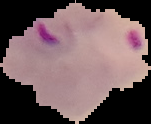
Malaria status: parasitized. Image is 151×124 pixels. From a thin blood smear. The area outside the segmented cell region is set to black.